State which parasite is depicted.
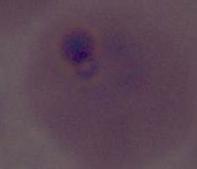

This is Plasmodium.

magnification = 400x or 1000x
modality = photomicrograph